Report the malaria status of this cell.
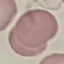
Uninfected.

Acquired by smartphone through the microscope eyepiece. Automatically extracted cell patch, resized to 64 × 64 pixels. Thin blood smear. Giemsa-stained preparation.